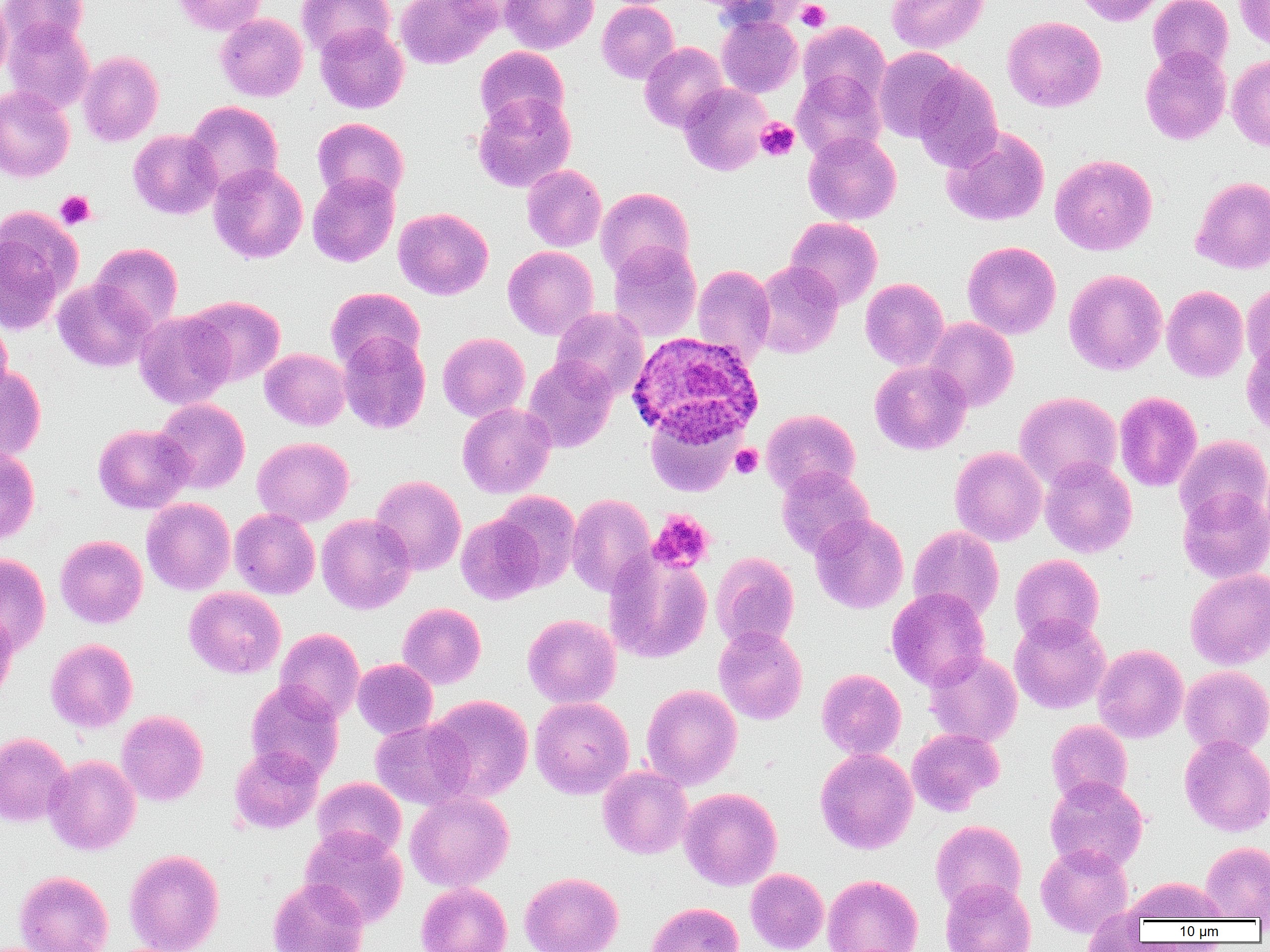
Summary:
  - Coordinate format: approximate bounding boxes as named x1/y1/x2/y2 corners in pixels
  - Plasmodium ovale-infected red blood cell locations: (x1=627, y1=331, x2=764, y2=445)
  - Platelet locations (subset): (x1=796, y1=0, x2=831, y2=31), (x1=755, y1=118, x2=800, y2=161), (x1=55, y1=190, x2=96, y2=229), (x1=730, y1=444, x2=763, y2=478)
  - Uninfected red blood cell locations (subset): (x1=0, y1=0, x2=12, y2=83), (x1=1, y1=0, x2=88, y2=51), (x1=171, y1=0, x2=268, y2=36), (x1=296, y1=0, x2=395, y2=59), (x1=395, y1=0, x2=498, y2=69), (x1=500, y1=0, x2=598, y2=53), (x1=711, y1=0, x2=808, y2=32), (x1=887, y1=0, x2=989, y2=53), (x1=1074, y1=0, x2=1165, y2=26), (x1=1147, y1=0, x2=1233, y2=75), (x1=1234, y1=0, x2=1270, y2=50), (x1=597, y1=1, x2=680, y2=84), (x1=215, y1=13, x2=308, y2=101), (x1=717, y1=14, x2=802, y2=97), (x1=1003, y1=16, x2=1106, y2=112), (x1=3, y1=19, x2=94, y2=114), (x1=798, y1=21, x2=890, y2=105), (x1=315, y1=23, x2=409, y2=113), (x1=639, y1=42, x2=728, y2=133), (x1=475, y1=46, x2=569, y2=131), (x1=1140, y1=46, x2=1231, y2=145), (x1=873, y1=47, x2=964, y2=142), (x1=78, y1=51, x2=164, y2=146), (x1=1227, y1=54, x2=1270, y2=152), (x1=911, y1=64, x2=1004, y2=171), (x1=792, y1=70, x2=886, y2=160), (x1=678, y1=83, x2=771, y2=176), (x1=0, y1=86, x2=75, y2=183), (x1=473, y1=93, x2=576, y2=192), (x1=184, y1=101, x2=283, y2=197), (x1=312, y1=117, x2=409, y2=204), (x1=942, y1=127, x2=1050, y2=226), (x1=128, y1=129, x2=222, y2=219), (x1=803, y1=131, x2=901, y2=225), (x1=1050, y1=154, x2=1157, y2=255), (x1=208, y1=163, x2=308, y2=263), (x1=521, y1=164, x2=607, y2=252), (x1=307, y1=173, x2=399, y2=267), (x1=1190, y1=176, x2=1270, y2=274), (x1=596, y1=187, x2=694, y2=280), (x1=394, y1=207, x2=493, y2=300), (x1=0, y1=208, x2=80, y2=332), (x1=784, y1=216, x2=883, y2=309), (x1=962, y1=241, x2=1061, y2=339), (x1=91, y1=242, x2=183, y2=333), (x1=608, y1=242, x2=701, y2=342), (x1=503, y1=246, x2=599, y2=340), (x1=752, y1=261, x2=843, y2=359), (x1=693, y1=264, x2=776, y2=362), (x1=1064, y1=269, x2=1167, y2=375), (x1=860, y1=278, x2=949, y2=372), (x1=52, y1=279, x2=155, y2=372), (x1=1242, y1=280, x2=1270, y2=373), (x1=1162, y1=285, x2=1249, y2=382), (x1=325, y1=287, x2=424, y2=372), (x1=186, y1=295, x2=285, y2=386), (x1=551, y1=307, x2=648, y2=400), (x1=134, y1=310, x2=235, y2=409), (x1=0, y1=316, x2=13, y2=403), (x1=924, y1=317, x2=1018, y2=411), (x1=338, y1=332, x2=431, y2=434), (x1=437, y1=332, x2=529, y2=422), (x1=1241, y1=337, x2=1270, y2=440), (x1=259, y1=348, x2=350, y2=430), (x1=523, y1=356, x2=617, y2=452), (x1=869, y1=360, x2=971, y2=455), (x1=0, y1=363, x2=46, y2=461), (x1=1014, y1=391, x2=1122, y2=490), (x1=1114, y1=391, x2=1202, y2=491), (x1=153, y1=398, x2=250, y2=494), (x1=457, y1=402, x2=556, y2=498), (x1=645, y1=408, x2=743, y2=496), (x1=761, y1=409, x2=860, y2=497), (x1=93, y1=424, x2=193, y2=514), (x1=1174, y1=435, x2=1270, y2=528), (x1=252, y1=437, x2=354, y2=526), (x1=950, y1=446, x2=1047, y2=546), (x1=0, y1=447, x2=40, y2=545), (x1=1039, y1=456, x2=1138, y2=558), (x1=776, y1=465, x2=874, y2=558), (x1=370, y1=475, x2=466, y2=574), (x1=1177, y1=487, x2=1269, y2=584), (x1=493, y1=491, x2=581, y2=589), (x1=566, y1=493, x2=656, y2=596), (x1=141, y1=498, x2=235, y2=595), (x1=229, y1=508, x2=320, y2=599), (x1=809, y1=513, x2=909, y2=613), (x1=316, y1=514, x2=416, y2=614), (x1=455, y1=514, x2=545, y2=605), (x1=908, y1=525, x2=1004, y2=622), (x1=55, y1=535, x2=147, y2=628), (x1=604, y1=551, x2=712, y2=663), (x1=711, y1=552, x2=799, y2=650), (x1=0, y1=553, x2=51, y2=655), (x1=1010, y1=554, x2=1105, y2=645), (x1=1185, y1=569, x2=1270, y2=669), (x1=184, y1=586, x2=286, y2=678), (x1=887, y1=587, x2=991, y2=690), (x1=397, y1=602, x2=486, y2=689), (x1=0, y1=609, x2=18, y2=705), (x1=523, y1=614, x2=621, y2=708), (x1=1009, y1=614, x2=1111, y2=714), (x1=714, y1=626, x2=808, y2=725), (x1=275, y1=628, x2=364, y2=722), (x1=45, y1=639, x2=138, y2=732), (x1=1093, y1=643, x2=1189, y2=743), (x1=924, y1=651, x2=1023, y2=746), (x1=353, y1=659, x2=438, y2=739), (x1=1180, y1=665, x2=1270, y2=756), (x1=816, y1=668, x2=906, y2=760), (x1=245, y1=680, x2=345, y2=781), (x1=641, y1=684, x2=742, y2=789), (x1=426, y1=694, x2=533, y2=802), (x1=530, y1=696, x2=634, y2=798), (x1=116, y1=710, x2=208, y2=805), (x1=370, y1=719, x2=474, y2=809), (x1=1046, y1=719, x2=1133, y2=805), (x1=906, y1=728, x2=1004, y2=815), (x1=0, y1=732, x2=73, y2=827), (x1=1180, y1=734, x2=1270, y2=836), (x1=229, y1=745, x2=323, y2=833), (x1=815, y1=748, x2=917, y2=853), (x1=44, y1=755, x2=141, y2=855), (x1=597, y1=766, x2=693, y2=859), (x1=1045, y1=776, x2=1148, y2=873), (x1=313, y1=777, x2=407, y2=860), (x1=679, y1=787, x2=782, y2=890), (x1=405, y1=790, x2=514, y2=892), (x1=930, y1=819, x2=1027, y2=912), (x1=300, y1=826, x2=408, y2=927), (x1=1200, y1=841, x2=1270, y2=920), (x1=1035, y1=842, x2=1133, y2=936), (x1=123, y1=848, x2=224, y2=952), (x1=745, y1=868, x2=829, y2=952), (x1=14, y1=871, x2=113, y2=952), (x1=519, y1=871, x2=623, y2=952), (x1=822, y1=874, x2=923, y2=952), (x1=1125, y1=877, x2=1227, y2=923), (x1=267, y1=878, x2=369, y2=952), (x1=940, y1=879, x2=1036, y2=952), (x1=416, y1=882, x2=512, y2=952), (x1=646, y1=901, x2=744, y2=952), (x1=1082, y1=909, x2=1147, y2=952)
  - Slide-level diagnosis: Plasmodium ovale
  - Image size: 1270×952 pixels
  - Modality: light microscopy
  - Preparation: thin blood film
  - Field of view: single
  - Magnification: 1000x